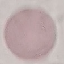
Summary:
  - Result: no malaria parasites detected
  - Image type: cell patch, automatically extracted from a larger field of view and resized to 64 × 64 pixels
  - Preparation: thin blood film
  - Capture: smartphone through the microscope eyepiece
  - Stain: Giemsa